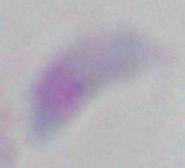
Micrograph. Toxoplasma gondii is seen. 1000x magnification.